Report the malaria status of this cell.
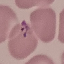

It is parasitized.

Summary:
  - Preparation: thin smear
  - Capture: smartphone through the microscope eyepiece
  - Stain: Giemsa
  - Image type: automatically extracted cell patch, resized to 64 × 64 pixels